Assess this cell for malaria.
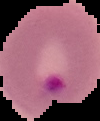

Parasitized.

preparation = thin blood smear
image type = segmented cell region on a black background
image size = 100×121 pixels